Outline each blood parasite and name the species.
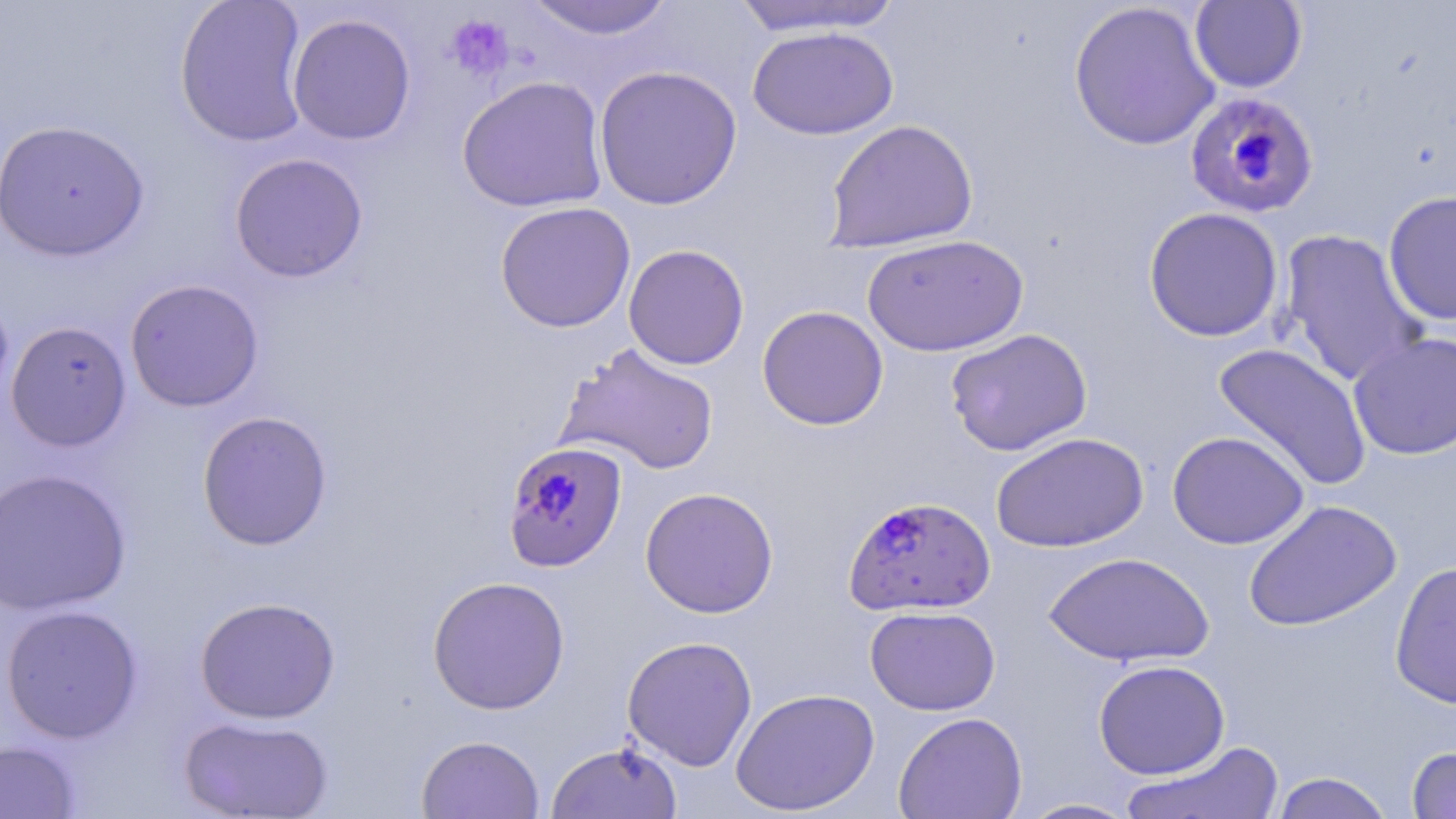
Approximate bounding boxes as [x1, y1, x2, y2] in pixels.
Plasmodium falciparum-infected red blood cells: [1184, 90, 1319, 219], [503, 441, 628, 573], [843, 494, 995, 617].
No Plasmodium ovale, Plasmodium malariae, Plasmodium vivax, Babesia divergens, or Trypanosoma brucei observed.

slide_level_diagnosis: Plasmodium falciparum
field_of_view: one of a larger specimen
preparation: thin blood smear
modality: light microscopy
magnification: 1000x
stain: May-Grünwald-Giemsa
uninfected_red_blood_cell_locations: 'approximate bounding boxes as [x1, y1, x2, y2] in pixels: [173, 0, 312, 148], [522, 0, 677, 40], [730, 1, 907, 38], [1069, 1, 1221, 152], [1190, 1, 1307, 93], [287, 13, 417, 146], [747, 26, 898, 140], [593, 65, 743, 211], [456, 75, 609, 213], [0, 118, 151, 261], [823, 118, 979, 253], [229, 153, 368, 282], [1383, 190, 1456, 326], [495, 201, 635, 332], [1143, 207, 1284, 342], [1277, 229, 1430, 388], [861, 234, 1028, 356], [623, 244, 750, 370], [124, 278, 264, 412], [0, 288, 14, 412], [757, 305, 889, 431], [5, 320, 132, 452], [945, 328, 1092, 456], [1347, 331, 1456, 460], [556, 342, 720, 476], [1212, 342, 1373, 492], [197, 410, 333, 550], [1167, 430, 1309, 550], [991, 431, 1148, 552], [0, 467, 133, 615], [639, 486, 779, 618], [1243, 498, 1402, 632], [1044, 551, 1214, 667], [1390, 560, 1456, 708], [427, 575, 570, 714], [194, 596, 340, 724], [0, 604, 143, 743], [865, 605, 1000, 716], [621, 635, 758, 771], [1093, 659, 1230, 779], [729, 687, 880, 816], [893, 711, 1027, 819], [179, 714, 335, 818], [416, 734, 544, 819], [0, 740, 81, 818], [546, 740, 683, 819], [1119, 740, 1288, 819], [1406, 745, 1456, 818], [1269, 772, 1396, 818], [1016, 798, 1141, 818]'
image_size: 1456×819 pixels
platelet_locations: 'approximate bounding boxes as [x1, y1, x2, y2] in pixels: [445, 14, 515, 83]'